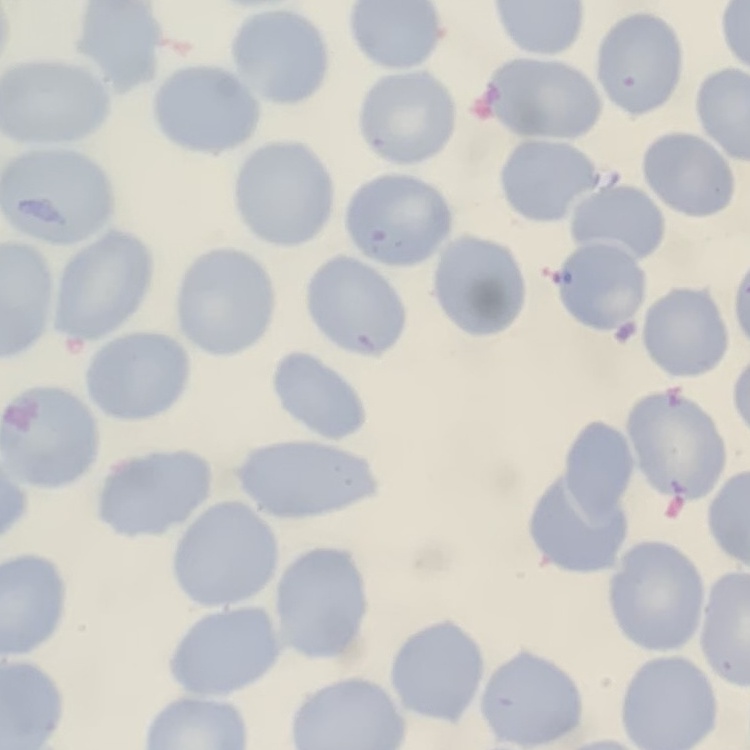

Summary:
  - Erythrocyte morphology: no rouleaux formation
  - Image type: square crop of a larger photomicrograph
  - Preparation: thin blood smear
  - Stain: Field's or Giemsa